Mark where platelets are.
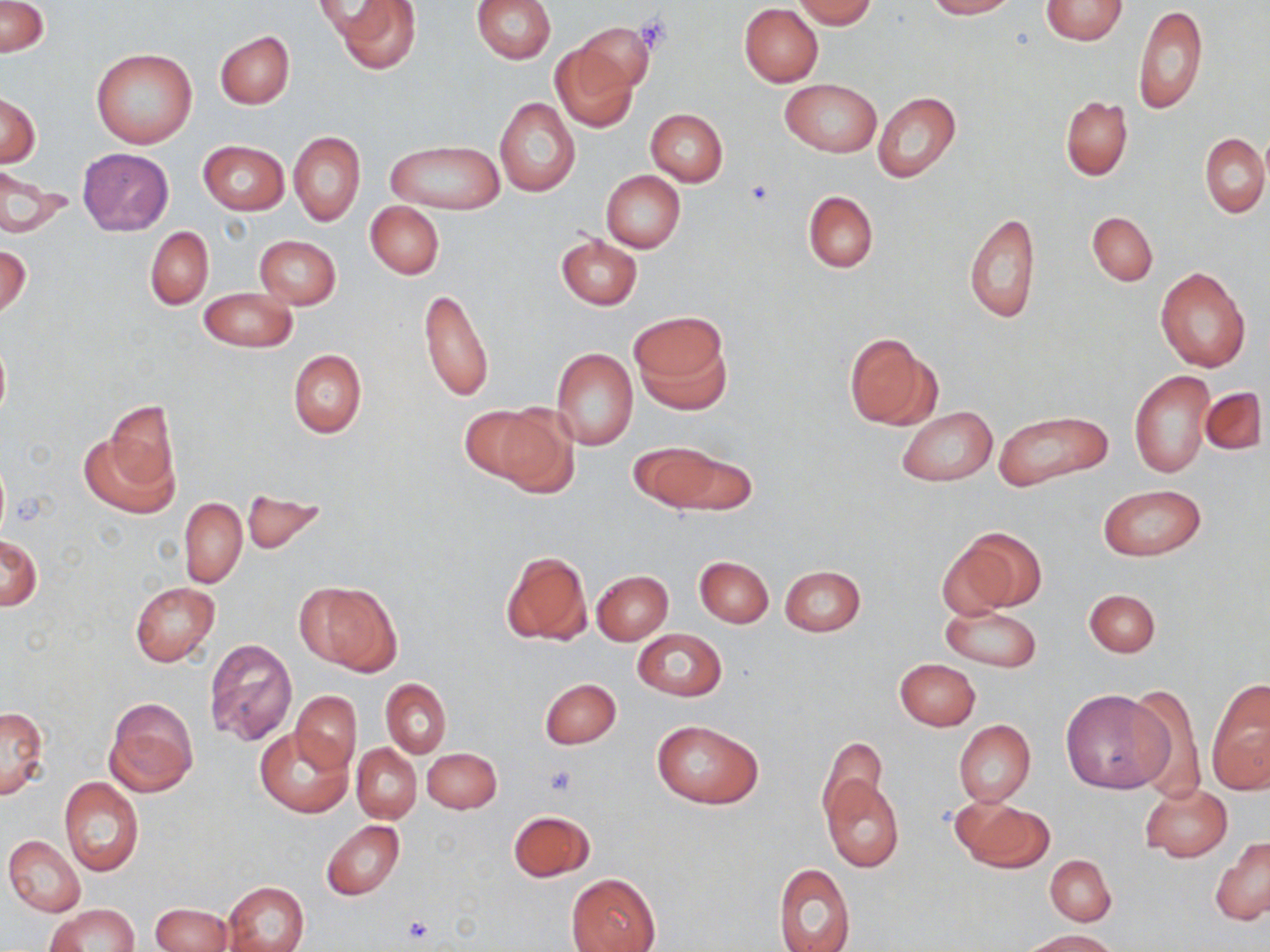

Approximate bounding boxes as (x1, y1, x2, y2) in pixels.
Platelets: (635, 13, 676, 53), (745, 179, 776, 207), (543, 764, 577, 796), (399, 915, 434, 945).

Summary:
  - Uninfected red blood cell locations: (1, 0, 49, 57), (329, 0, 422, 73), (472, 0, 556, 62), (793, 0, 877, 28), (926, 0, 1016, 18), (1040, 0, 1129, 44), (739, 4, 823, 86), (1134, 4, 1208, 115), (579, 22, 654, 96), (215, 30, 295, 109), (550, 43, 638, 133), (92, 48, 198, 148), (781, 79, 880, 157), (873, 92, 961, 184), (0, 94, 41, 166), (1060, 96, 1133, 180), (493, 97, 579, 196), (646, 109, 727, 186), (1257, 130, 1270, 202), (289, 131, 365, 226), (1200, 134, 1269, 218), (386, 139, 505, 216), (198, 141, 289, 215), (76, 148, 173, 236), (0, 166, 70, 240), (601, 171, 685, 252), (803, 190, 878, 272), (365, 202, 444, 279), (1087, 211, 1157, 286), (963, 213, 1040, 324), (146, 226, 213, 308), (556, 234, 642, 310), (254, 235, 342, 309), (1, 246, 31, 320), (1155, 266, 1252, 374), (418, 286, 494, 403), (198, 288, 297, 352), (632, 311, 730, 412), (845, 333, 937, 430), (0, 334, 10, 424), (550, 348, 638, 451), (288, 350, 367, 438), (1130, 370, 1214, 479), (1202, 386, 1267, 456), (103, 401, 177, 493), (477, 403, 576, 493), (896, 406, 998, 486), (992, 408, 1114, 491), (81, 428, 178, 519), (630, 441, 731, 511), (1100, 484, 1205, 560), (241, 488, 326, 556), (179, 497, 247, 587), (959, 528, 1045, 612), (0, 536, 42, 610), (501, 551, 591, 647), (695, 556, 773, 627), (779, 565, 866, 636), (593, 571, 673, 644), (129, 581, 221, 667), (297, 581, 401, 677), (1085, 589, 1160, 658), (939, 605, 1043, 672), (632, 629, 727, 701), (204, 639, 297, 746), (895, 659, 980, 730), (540, 677, 621, 750), (381, 679, 451, 757), (1128, 682, 1206, 801), (1207, 682, 1270, 794), (1060, 690, 1173, 794), (290, 691, 361, 772), (104, 698, 198, 796), (1, 706, 49, 801), (954, 719, 1035, 807), (652, 720, 762, 808), (255, 727, 352, 817), (817, 735, 889, 825), (352, 743, 421, 823), (422, 748, 501, 813), (822, 775, 903, 872), (59, 778, 144, 879), (1140, 783, 1232, 862), (955, 795, 1054, 872), (508, 809, 595, 882), (321, 820, 405, 899), (4, 835, 85, 917), (1210, 837, 1270, 925), (1046, 855, 1117, 926), (773, 862, 855, 952), (566, 873, 661, 952), (223, 881, 308, 952), (45, 903, 139, 951), (149, 903, 234, 952), (1022, 929, 1122, 951)
  - Slide-level diagnosis: no evidence of blood parasites
  - Field of view: single
  - Magnification: 1000x
  - Preparation: thin blood smear
  - Image size: 1270×952 pixels
  - Stain: May-Grünwald-Giemsa
  - Modality: light microscopy